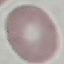

Malaria status: uninfected. Automatically extracted cell patch, resized to 64 × 64 pixels. Giemsa-stained preparation. Thin blood film. Photographed with a smartphone camera at the microscope eyepiece.